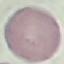
Result: no malaria parasites detected. Acquired by smartphone through the microscope eyepiece. Cell patch, automatically extracted from a larger field of view and resized to 64 × 64 pixels. Thin smear of blood. Giemsa-stained preparation.